Give the preparation type.
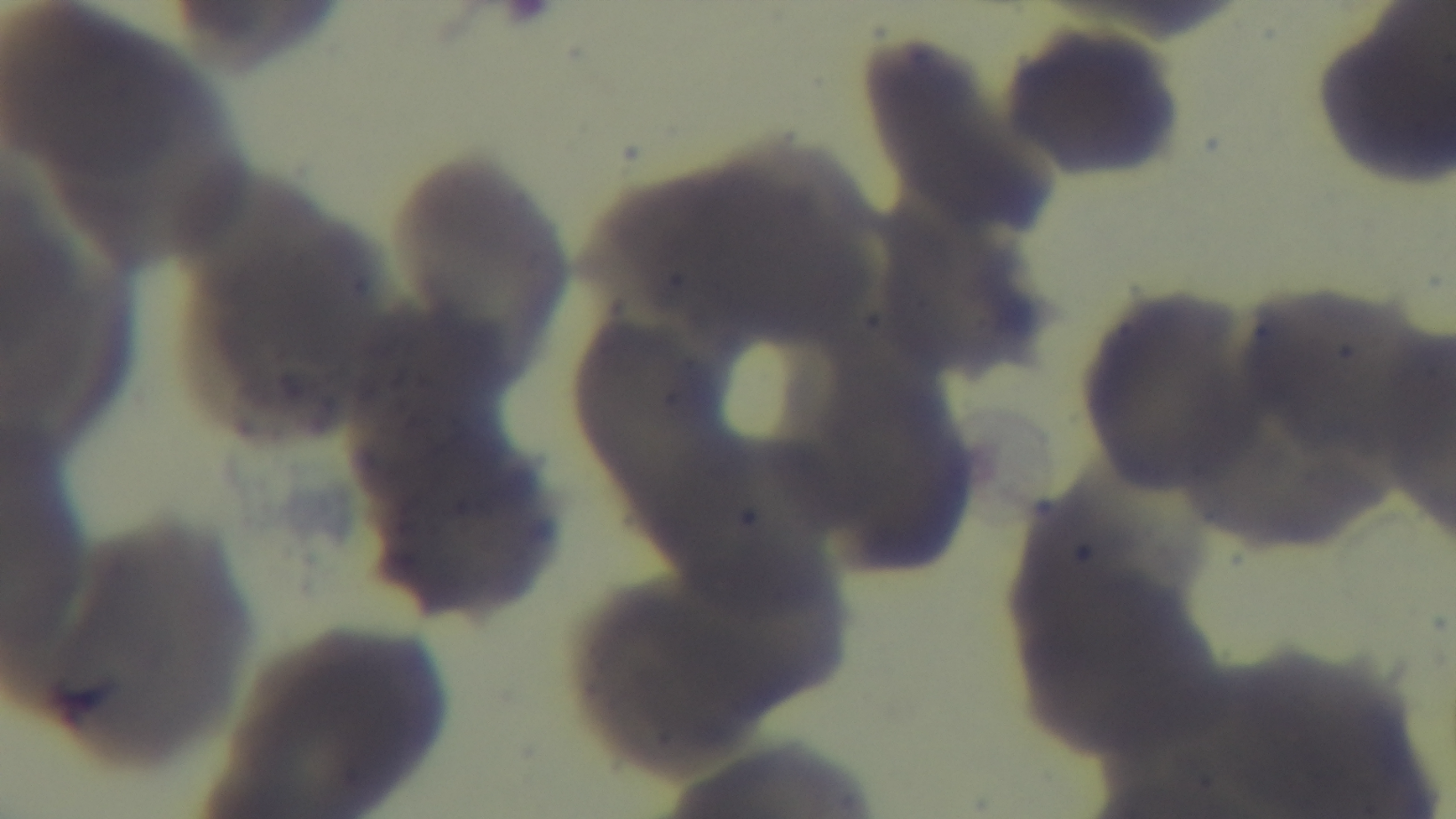
A thin smear.

stain = Giemsa
objective = 100x oil immersion
malaria status = uninfected
field of view = one from the slide
modality = light microscopy
capture = mounted 4K digital camera